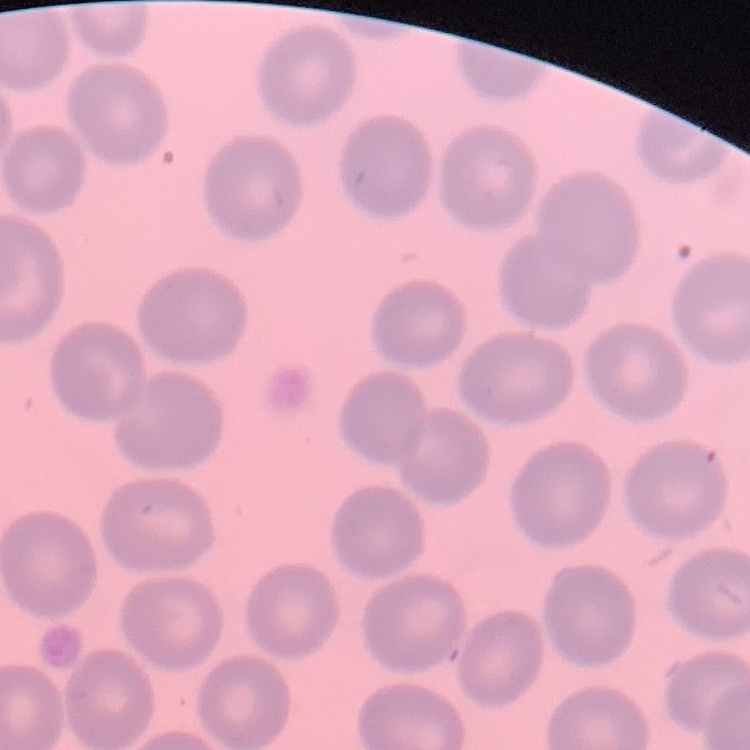

{
  "red_blood_cell_morphology": "no rouleaux formation",
  "image_type": "square crop of a larger photomicrograph",
  "preparation": "thin blood smear",
  "stain": "Field's or Giemsa"
}